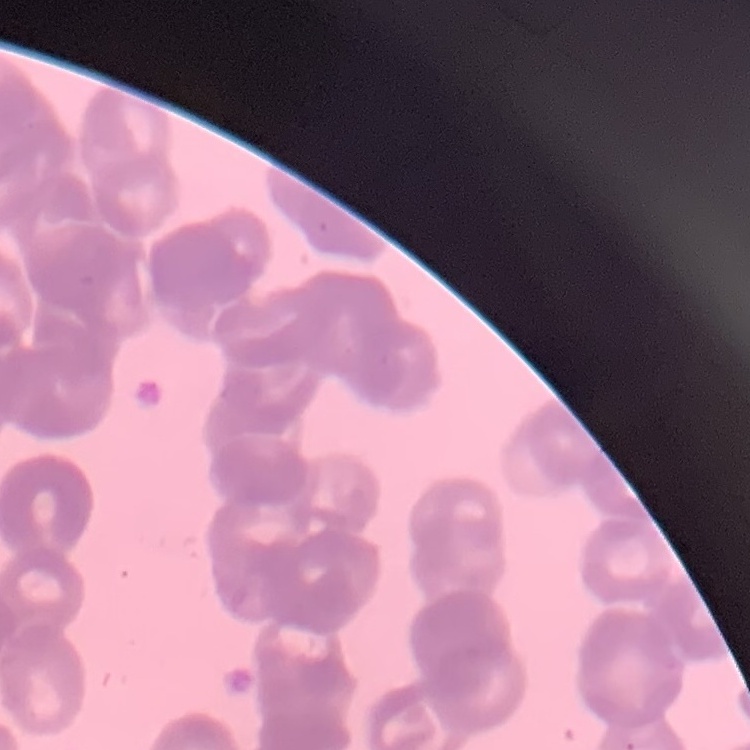 The erythrocytes show rouleaux formation. Field's or Giemsa stain. Thin blood smear. One tile cut from a larger photomicrograph.